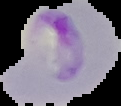
Summary:
  - Result: malaria parasites identified
  - Image type: cell region segmented out of the field of view; surrounding area masked to black
  - Image size: 121×106 pixels
  - Preparation: thin blood film